Report the malaria status of this cell.
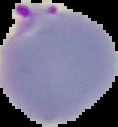

Parasitized.

From a thin blood smear. Image is 118×127 pixels. Cell region segmented out of the field of view; the surrounding area is masked to black.